Outline each uninfected red blood cell.
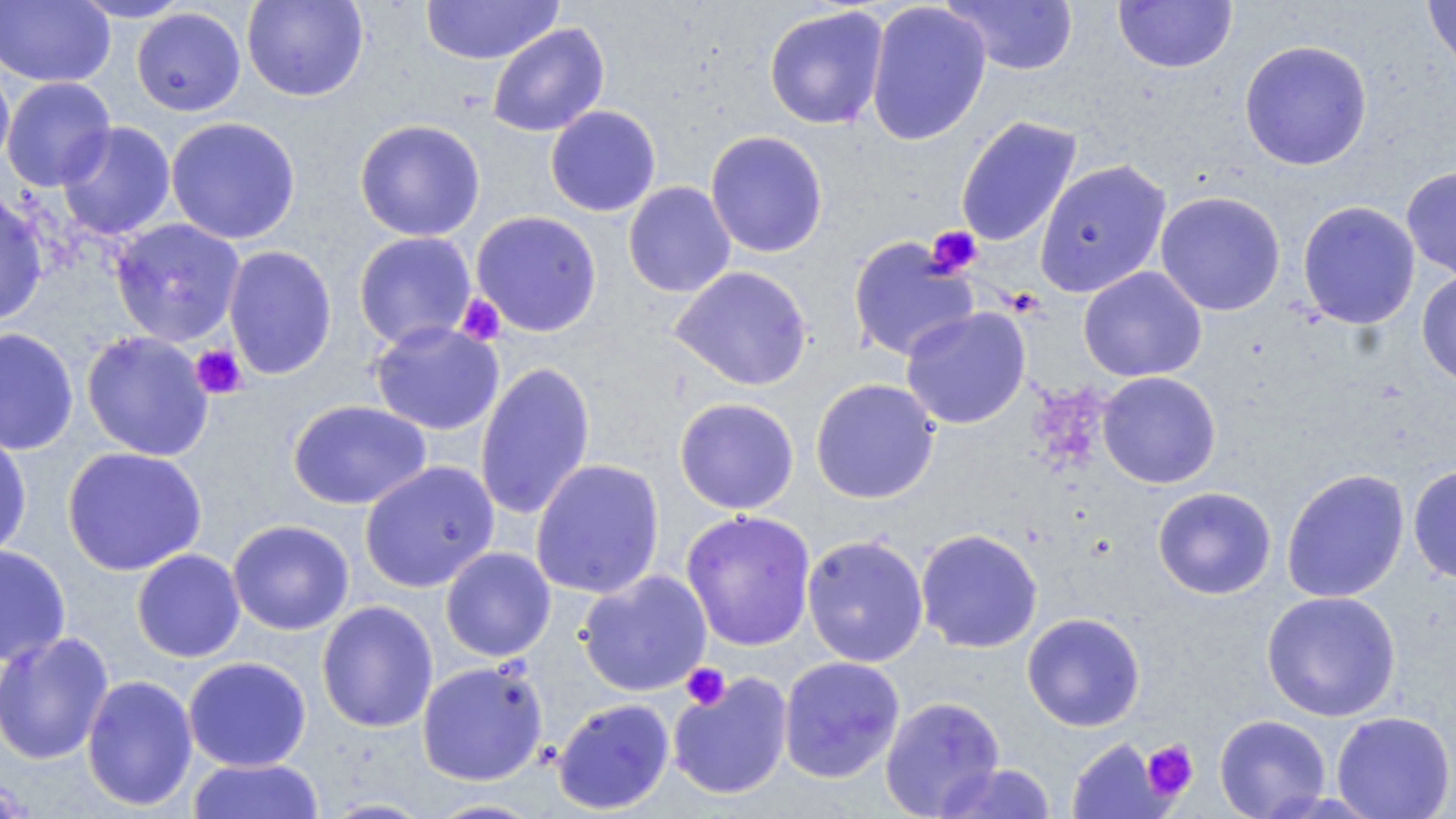

Approximate bounding boxes as (x1,y1)-(x2,y2) corner pairs in pixels.
Uninfected red blood cells: (0,0)-(114,88), (69,0)-(194,22), (241,0)-(369,102), (420,0)-(563,65), (942,0)-(1079,76), (1423,0)-(1456,81), (865,1)-(992,146), (1113,1)-(1237,73), (763,5)-(889,130), (131,7)-(246,116), (487,23)-(610,138), (1239,40)-(1372,170), (0,61)-(15,176), (1,76)-(117,191), (545,104)-(661,217), (955,115)-(1082,247), (166,116)-(301,245), (354,119)-(486,242), (56,121)-(176,241), (705,130)-(829,258), (1034,159)-(1172,298), (1401,165)-(1456,281), (623,181)-(736,298), (0,190)-(49,326), (1155,191)-(1286,316), (1297,200)-(1420,329), (470,210)-(602,337), (109,218)-(246,346), (353,231)-(477,349), (848,237)-(979,361), (223,245)-(338,380), (669,266)-(813,391), (1078,266)-(1207,382), (1417,268)-(1456,388), (900,306)-(1031,429), (369,321)-(504,435), (0,327)-(79,456), (81,330)-(214,461), (475,362)-(595,520), (1097,371)-(1221,489), (810,378)-(940,504), (674,397)-(799,514), (287,399)-(431,510), (0,429)-(33,559), (62,446)-(207,576), (530,458)-(665,600), (359,460)-(499,593), (1408,464)-(1456,584), (1281,468)-(1409,603), (1152,486)-(1277,600), (681,509)-(817,651), (227,519)-(354,635), (915,528)-(1043,654), (802,535)-(929,667), (0,544)-(71,667), (441,546)-(556,662), (131,548)-(245,663), (577,570)-(712,697), (1261,590)-(1402,722), (316,600)-(438,733), (1021,613)-(1146,732), (0,631)-(115,765), (183,656)-(311,772), (778,656)-(905,783), (416,660)-(548,786), (668,672)-(793,800), (81,674)-(198,811), (879,696)-(1005,818), (552,697)-(675,814), (1331,711)-(1456,819), (1214,714)-(1331,819), (1066,737)-(1170,819), (187,758)-(324,818), (933,761)-(1058,818), (423,797)-(549,818).

slide-level diagnosis = Plasmodium falciparum
preparation = thin blood film
field of view = single
platelet locations = approximate bounding boxes as (x1,y1)-(x2,y2) corner pairs in pixels: (926,226)-(982,278), (454,294)-(506,346), (190,344)-(247,399), (681,662)-(731,711), (1141,739)-(1198,802)
modality = light microscopy
image size = 1456×819 pixels
magnification = 1000x
stain = May-Grünwald-Giemsa